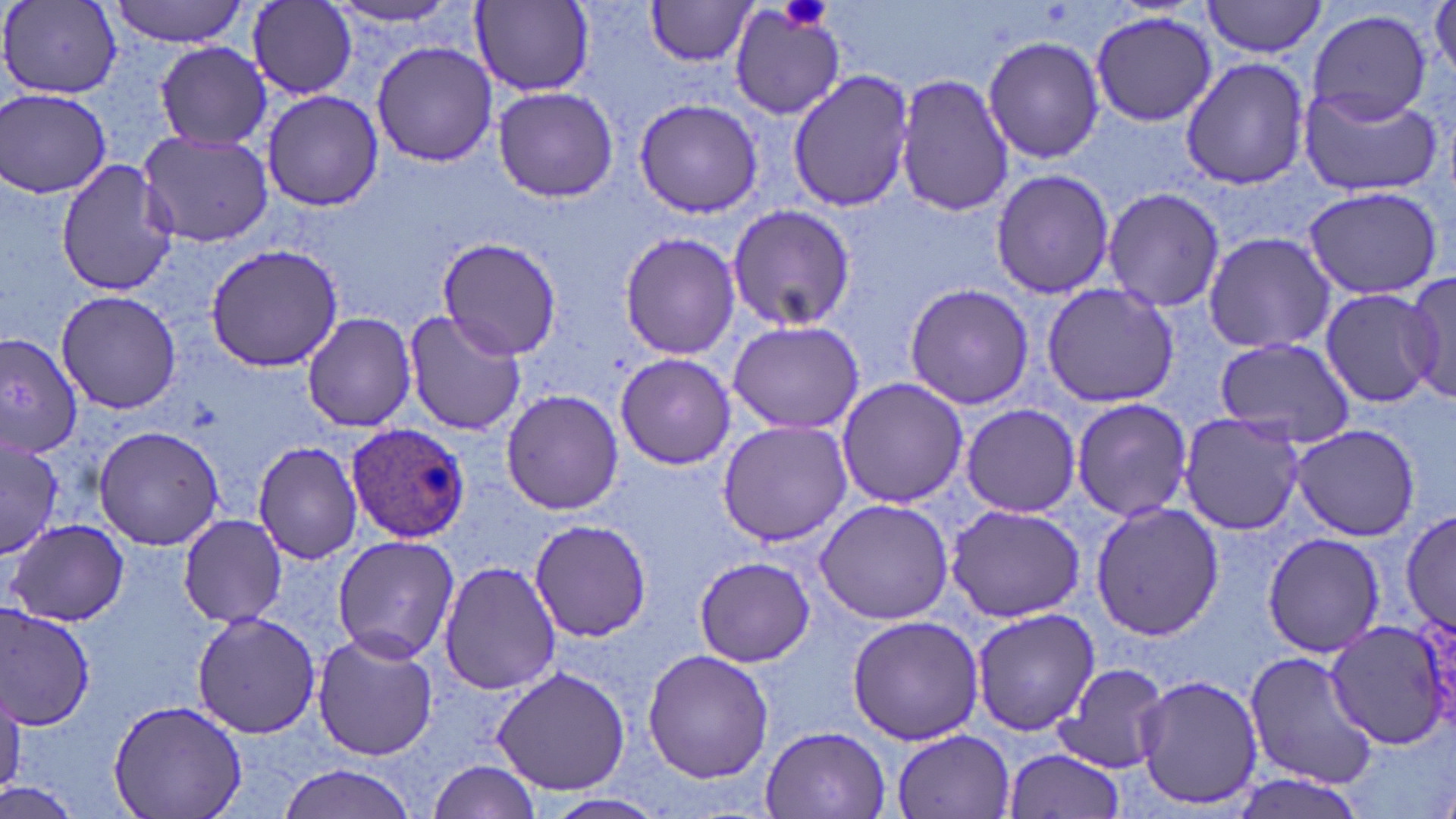

Summary:
  - Coordinate format: approximate bounding boxes as (x1, y1, x2, y2) in pixels
  - Uninfected red blood cell locations: (106, 0, 250, 46), (644, 0, 761, 67), (1202, 0, 1326, 58), (247, 1, 357, 97), (471, 1, 594, 94), (321, 2, 474, 30), (1428, 2, 1456, 79), (1, 3, 125, 99), (729, 5, 846, 121), (1307, 8, 1432, 124), (1090, 11, 1216, 128), (981, 35, 1104, 166), (155, 41, 272, 150), (372, 41, 497, 167), (1180, 57, 1311, 192), (786, 68, 915, 213), (894, 73, 1014, 217), (1297, 83, 1444, 196), (492, 86, 619, 202), (1, 88, 113, 199), (260, 90, 383, 210), (633, 97, 765, 219), (136, 129, 273, 245), (56, 160, 181, 296), (989, 169, 1115, 300), (1303, 185, 1443, 301), (1102, 186, 1224, 313), (726, 204, 855, 333), (1201, 231, 1335, 354), (618, 232, 741, 359), (435, 238, 562, 360), (205, 244, 346, 372), (1403, 269, 1456, 406), (1041, 282, 1179, 409), (902, 283, 1034, 410), (1318, 286, 1439, 410), (55, 288, 184, 415), (402, 309, 525, 436), (301, 312, 416, 432), (727, 319, 864, 435), (0, 331, 81, 461), (1211, 337, 1356, 449), (614, 353, 735, 469), (834, 377, 968, 508), (499, 389, 625, 515), (1071, 397, 1194, 523), (961, 403, 1081, 517), (1176, 411, 1308, 535), (717, 421, 853, 546), (92, 424, 225, 551), (1289, 424, 1421, 541), (1, 436, 62, 558), (252, 441, 364, 566), (814, 496, 954, 625), (1090, 499, 1222, 641), (946, 503, 1086, 624), (1398, 508, 1456, 636), (176, 513, 289, 628), (528, 518, 652, 642), (7, 519, 130, 627), (1262, 532, 1387, 658), (331, 536, 460, 664), (694, 557, 815, 667), (439, 560, 560, 695), (0, 604, 99, 728), (972, 608, 1100, 736), (191, 610, 321, 739), (846, 613, 986, 744), (1322, 619, 1456, 750), (311, 632, 440, 760), (642, 649, 773, 783), (1244, 650, 1379, 790), (1053, 663, 1170, 772), (489, 665, 630, 796), (1135, 673, 1261, 811), (0, 693, 26, 793), (108, 698, 247, 819), (760, 725, 891, 819), (890, 728, 1019, 819), (1002, 749, 1127, 819), (426, 760, 545, 816), (274, 763, 424, 819), (1231, 771, 1362, 819), (1, 780, 78, 819), (547, 792, 668, 817)
  - Platelet locations: (777, 0, 834, 32)
  - Plasmodium ovale-infected red blood cell locations: (346, 424, 472, 544)
  - Slide-level diagnosis: Plasmodium ovale
  - Modality: optical microscopy
  - Magnification: 1000x
  - Stain: May-Grünwald-Giemsa
  - Preparation: thin blood film
  - Image size: 1456×819 pixels
  - Field of view: one of a larger specimen